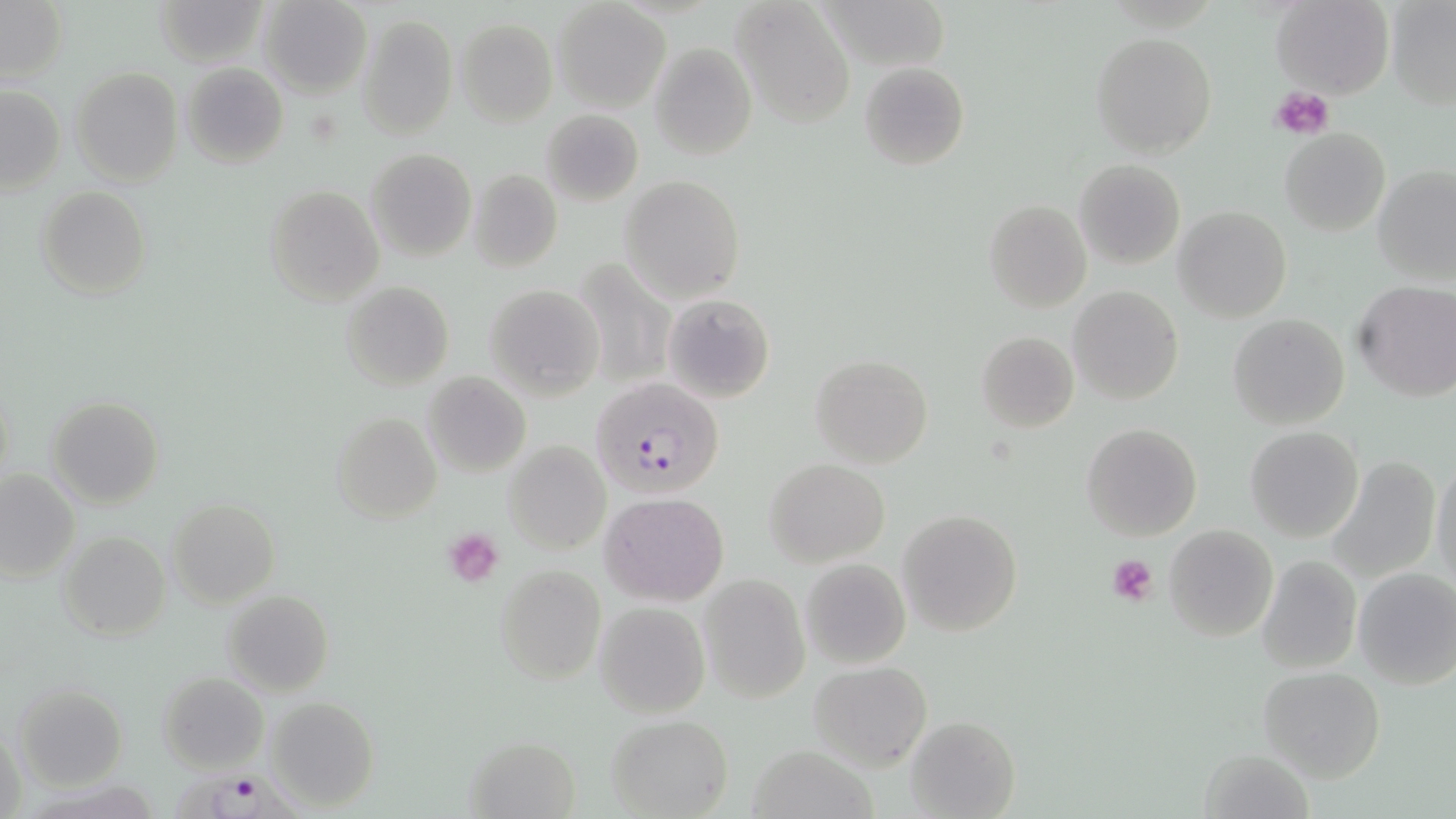

slide-level diagnosis = Plasmodium falciparum
platelet locations = approximate bounding boxes as [x1, y1, x2, y2] in pixels: [1272, 86, 1336, 141], [441, 528, 504, 586], [1106, 553, 1160, 607]
stain = May-Grünwald-Giemsa
modality = light microscopy
preparation = thin blood smear
uninfected red blood cell locations = approximate bounding boxes as [x1, y1, x2, y2] in pixels: [151, 0, 267, 68], [258, 0, 372, 98], [820, 0, 951, 72], [1386, 0, 1456, 110], [730, 1, 856, 128], [1271, 1, 1393, 96], [0, 2, 68, 84], [552, 2, 669, 111], [358, 13, 458, 140], [455, 18, 558, 127], [1090, 32, 1216, 157], [648, 42, 756, 163], [859, 61, 969, 170], [180, 64, 288, 168], [70, 67, 183, 187], [1, 84, 66, 194], [542, 109, 643, 206], [1280, 128, 1390, 236], [366, 148, 476, 261], [1074, 159, 1186, 269], [1373, 165, 1456, 283], [468, 169, 562, 273], [619, 176, 744, 301], [37, 185, 151, 300], [264, 185, 384, 306], [984, 200, 1093, 313], [1173, 206, 1292, 324], [587, 252, 678, 387], [341, 281, 453, 390], [1353, 282, 1456, 402], [485, 284, 605, 399], [1069, 285, 1183, 405], [662, 294, 775, 403], [1227, 314, 1349, 430], [975, 331, 1078, 432], [810, 353, 933, 468], [422, 371, 532, 477], [46, 395, 164, 508], [333, 412, 441, 524], [1081, 423, 1201, 540], [1245, 427, 1364, 543], [503, 440, 609, 555], [1328, 454, 1444, 583], [764, 458, 890, 566], [1431, 458, 1456, 587], [1, 468, 79, 584], [600, 491, 729, 605], [168, 499, 279, 607], [897, 509, 1023, 637], [1163, 524, 1279, 642], [58, 530, 169, 642], [1255, 554, 1361, 674], [800, 558, 911, 669], [495, 564, 606, 684], [1353, 567, 1456, 689], [698, 576, 810, 703], [223, 590, 333, 695], [595, 601, 710, 718], [807, 660, 933, 769], [1257, 666, 1386, 781], [158, 672, 267, 773], [14, 684, 127, 789], [264, 696, 378, 812], [606, 715, 733, 819], [904, 715, 1019, 819], [2, 726, 28, 815], [465, 734, 580, 817], [749, 744, 877, 819], [1200, 747, 1314, 819]
field of view = single
Plasmodium falciparum-infected red blood cell locations = approximate bounding boxes as [x1, y1, x2, y2] in pixels: [592, 376, 725, 499], [164, 760, 311, 819]
image size = 1456×819 pixels
magnification = 1000x